Locate every leukocyte (white blood cell).
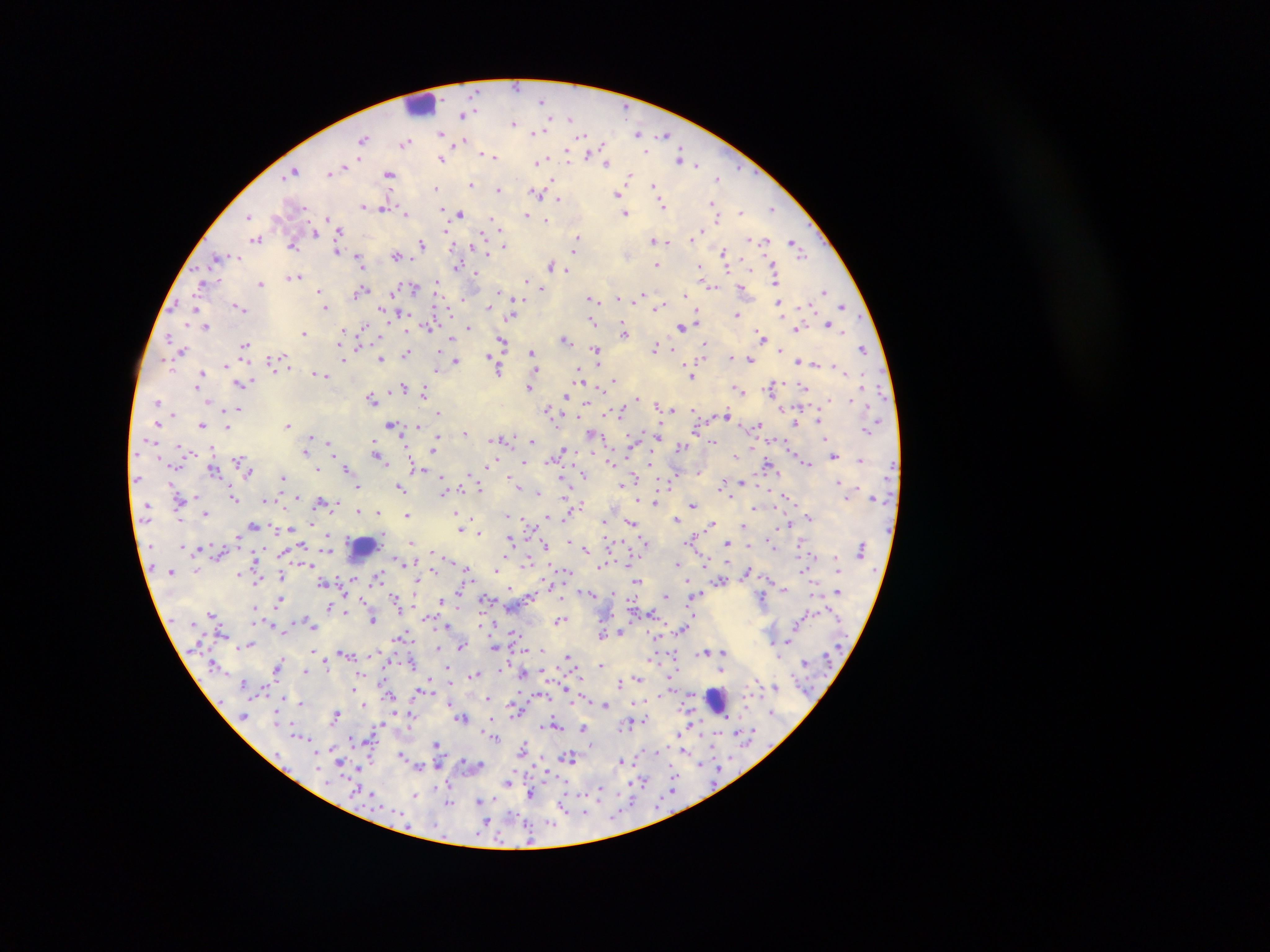
Approximate centers as [x, y] in pixels.
Leukocytes: [419, 104], [364, 549], [716, 699].

Malaria parasite locations: [544, 99], [465, 114], [514, 122], [539, 131], [639, 131], [441, 132], [664, 136], [364, 140], [462, 141], [406, 142], [596, 152], [485, 153], [491, 156], [567, 157], [602, 157], [442, 158], [681, 158], [539, 160], [607, 161], [695, 162], [293, 171], [330, 172], [390, 174], [630, 177], [718, 177], [472, 184], [655, 187], [435, 189], [499, 189], [537, 192], [618, 193], [557, 199], [712, 203], [662, 204], [363, 206], [384, 207], [773, 207], [740, 211], [444, 212], [406, 213], [460, 213], [625, 213], [527, 216], [532, 216], [249, 217], [718, 217], [328, 219], [545, 220], [497, 223], [446, 229], [315, 232], [339, 232], [701, 232], [257, 238], [578, 238], [693, 239], [654, 240], [665, 240], [763, 242], [422, 244], [294, 245], [504, 245], [796, 245], [576, 247], [338, 249], [487, 250], [724, 253], [397, 255], [218, 258], [726, 260], [360, 262], [551, 265], [655, 265], [458, 266], [701, 266], [727, 267], [568, 270], [475, 274], [294, 276], [776, 278], [526, 279], [437, 282], [260, 283], [203, 285], [711, 285], [742, 287], [413, 288], [542, 288], [320, 290], [824, 290], [362, 291], [499, 291], [393, 294], [686, 294], [642, 295], [464, 296], [513, 297], [617, 297], [592, 298], [779, 302], [811, 305], [843, 305], [239, 306], [489, 306], [660, 306], [326, 307], [195, 308], [736, 313], [402, 314], [511, 314], [387, 315], [698, 315], [696, 320], [593, 322], [828, 322], [830, 325], [682, 326], [206, 327], [429, 327], [469, 327], [343, 328], [798, 328], [363, 329], [843, 330], [304, 333], [624, 333], [762, 334], [170, 337], [451, 338], [565, 339], [502, 342], [245, 345], [704, 345], [656, 348], [864, 349], [596, 350], [781, 350], [181, 351], [407, 352], [532, 352], [491, 356], [731, 357], [381, 358], [283, 360], [343, 360], [456, 360], [750, 360], [273, 361], [798, 361], [815, 363], [227, 365], [834, 365], [498, 367], [437, 368], [535, 368], [580, 370], [318, 373], [202, 374], [324, 374], [580, 376], [691, 376], [614, 379], [200, 380], [241, 382], [530, 385], [772, 386], [803, 386], [402, 387], [424, 391], [740, 391], [566, 395], [373, 398], [637, 399], [158, 401], [829, 401], [586, 403], [667, 406], [238, 409], [671, 409], [549, 410], [621, 410], [439, 411], [726, 413], [819, 421], [158, 423], [288, 423], [797, 423], [392, 424], [758, 424], [202, 425], [417, 426], [227, 427], [867, 430], [464, 432], [592, 433], [658, 434], [496, 439], [505, 439], [634, 439], [309, 441], [532, 441], [376, 442], [331, 443], [714, 443], [435, 444], [682, 446], [211, 448], [307, 452], [562, 452], [240, 456], [834, 456], [379, 458], [494, 458], [861, 460], [383, 461], [611, 462], [525, 463], [808, 463], [768, 464], [348, 469], [214, 470], [318, 470], [421, 470], [699, 470], [250, 472], [584, 475], [282, 477], [563, 478], [636, 480], [838, 481], [743, 482], [172, 483], [724, 484], [624, 485], [519, 486], [359, 487], [400, 487], [479, 487], [443, 490], [537, 493], [195, 496], [298, 496], [233, 497], [785, 497], [789, 497], [268, 501], [325, 502], [332, 503], [655, 503], [693, 504], [576, 507], [756, 508], [360, 510], [377, 511], [206, 512], [456, 512], [408, 514], [508, 515], [548, 517], [678, 518], [810, 518], [181, 520], [605, 520], [632, 521], [311, 522], [711, 523], [790, 523], [530, 525], [744, 525], [255, 526], [290, 528], [461, 528], [479, 532], [238, 536], [329, 537], [694, 539], [511, 540], [569, 541], [646, 541], [410, 542], [545, 544], [727, 544], [301, 545], [585, 549], [431, 550], [328, 551], [527, 558], [450, 560], [631, 561], [677, 564], [703, 565], [601, 567], [196, 569], [498, 569], [433, 570], [468, 570], [803, 570], [748, 571], [240, 574], [281, 576], [353, 577], [379, 578], [720, 580], [638, 581], [323, 582], [688, 582], [551, 584], [416, 585], [509, 589], [783, 589], [837, 589], [589, 592], [697, 594], [530, 596], [666, 596], [441, 598], [561, 598], [762, 598], [396, 599], [486, 599], [281, 600], [633, 600], [255, 607], [330, 607], [345, 612], [694, 613], [213, 614], [649, 614], [801, 617], [373, 619], [560, 620], [255, 623], [448, 625], [314, 626], [680, 630], [621, 632], [514, 633], [602, 634], [400, 636], [789, 639], [251, 644], [495, 645], [460, 646], [438, 648], [312, 649], [542, 650], [707, 651], [345, 653], [373, 654], [724, 654], [568, 655], [674, 655], [654, 658], [280, 659], [326, 662], [601, 664], [279, 665], [448, 668], [306, 669], [722, 670], [524, 672], [475, 674], [638, 678], [244, 681], [430, 681], [620, 683], [353, 686], [776, 686], [566, 688], [266, 689], [543, 693], [656, 695], [488, 697], [301, 702], [449, 702], [363, 704], [605, 704], [517, 710], [393, 712], [336, 713], [411, 714], [462, 718], [646, 719], [552, 724], [584, 727], [680, 732], [739, 732], [494, 736], [350, 739], [436, 743], [316, 749], [524, 749], [683, 749], [402, 755], [570, 757], [622, 760], [441, 762], [480, 765], [359, 767], [717, 767], [674, 771], [509, 780], [641, 781], [449, 783], [599, 790], [673, 790], [531, 793], [415, 794], [493, 799], [631, 800], [480, 801], [449, 803], [563, 806], [584, 813], [487, 820], [551, 822]. Single field of view. Thick blood smear. Mobile-phone photograph taken through the microscope. Image is 1270×952 pixels. Sample from Ghana.